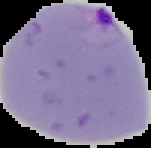
From a thin blood smear. Result: malaria parasites identified. Image is 151×148 pixels. Cell region segmented out of the field of view; the surrounding area is masked to black.